Classify this cell by malaria status.
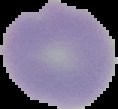
It is uninfected.

image_type: segmented cell region on a black background
preparation: thin blood film
image_size: 118×109 pixels